Assess this cell for malaria.
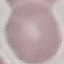

Uninfected.

Summary:
  - Stain: Giemsa
  - Image type: automatically extracted cell patch, resized to 64 × 64 pixels
  - Capture: smartphone through the microscope eyepiece
  - Preparation: thin smear